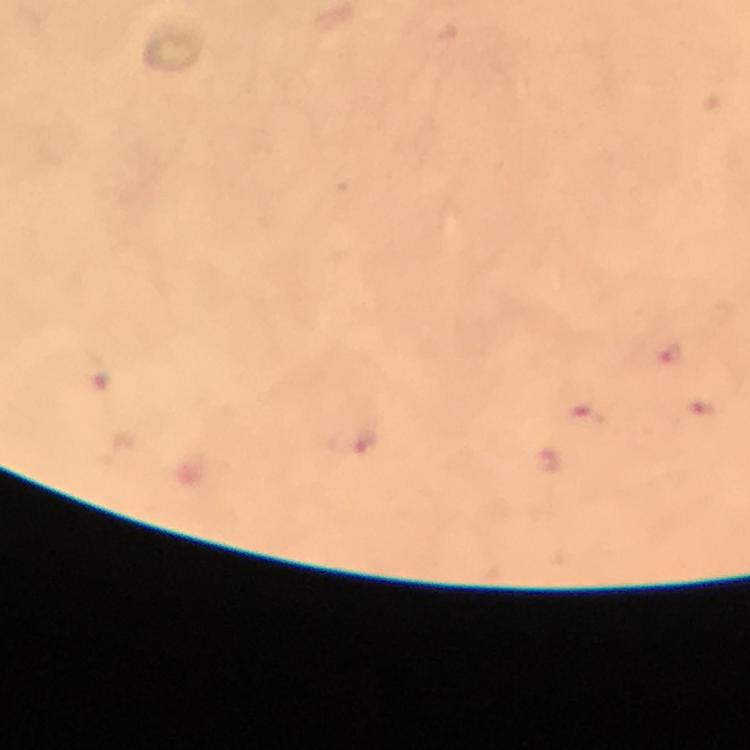
Approximate centers as {x, y} in pixels. Malaria parasite locations: {671, 355}, {698, 404}, {586, 421}, {364, 440}. At 100x magnification. Image is 750×750 pixels. Thick blood smear. A crop from one field of view. Giemsa-stained preparation. From a diagnostic examination for malaria. Immersion oil was used. Photographed with a smartphone mounted on the microscope.